Evaluate for Plasmodium parasites.
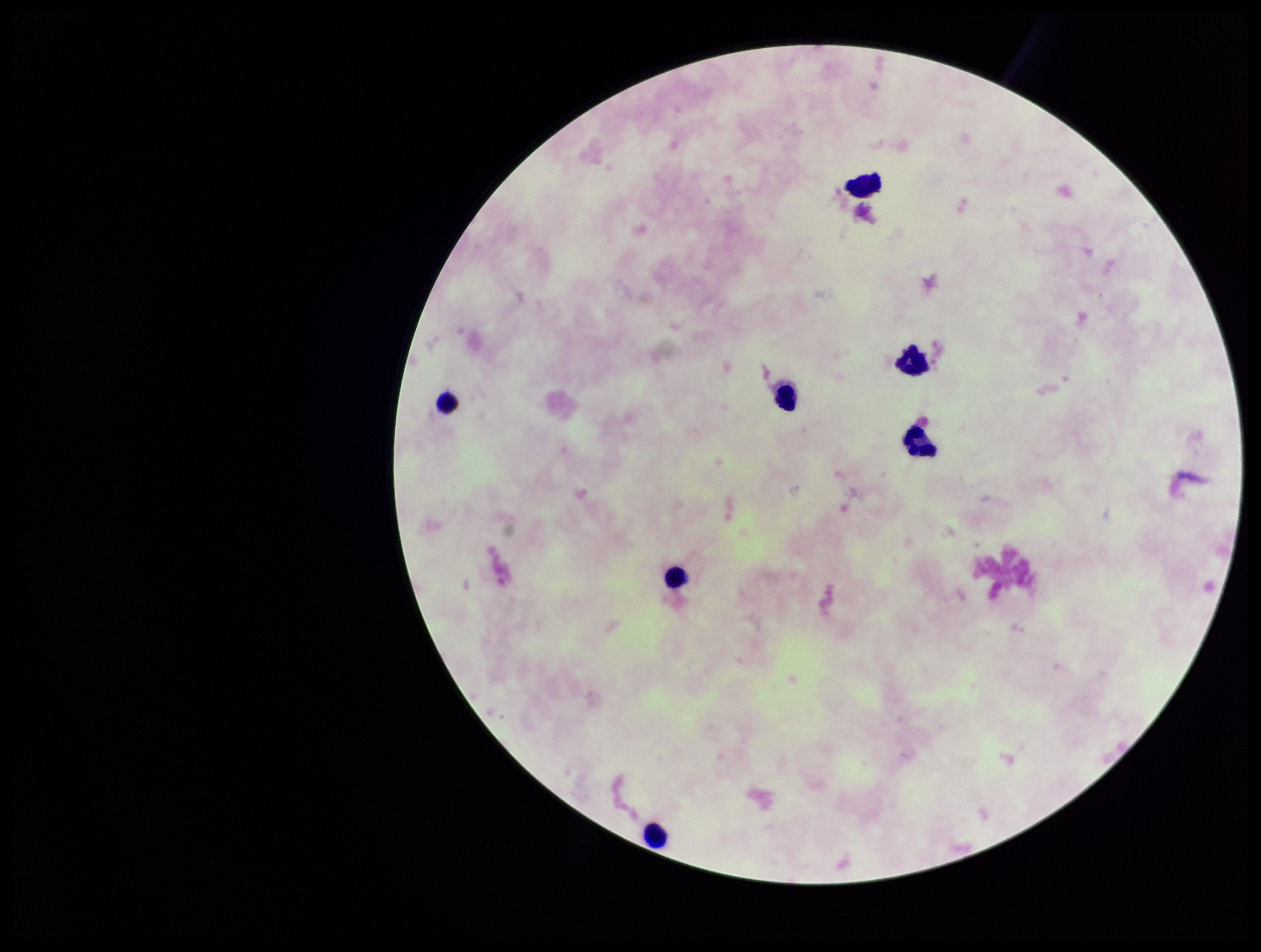
None detected.

parasite count = 0
preparation = thick blood smear
patient malaria status = negative
capture = smartphone photograph through the microscope eyepiece
field of view = one from this slide
leukocyte count = 7
image size = 1261×952 pixels
stain = Giemsa